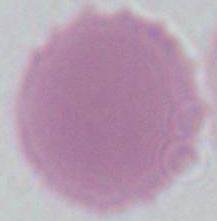 A red blood cell is shown. Micrograph. Captured at 1000x magnification.